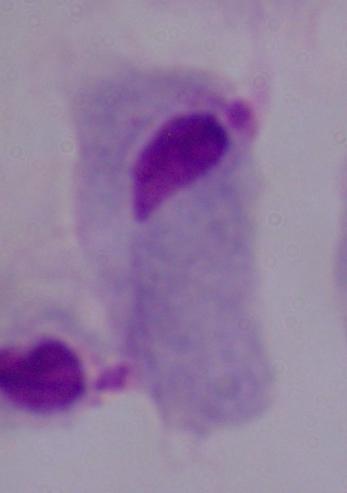
Summary:
  - Modality: photomicrograph
  - Magnification: 1000x
  - Identification: trichomonad